Locate every Plasmodium parasite.
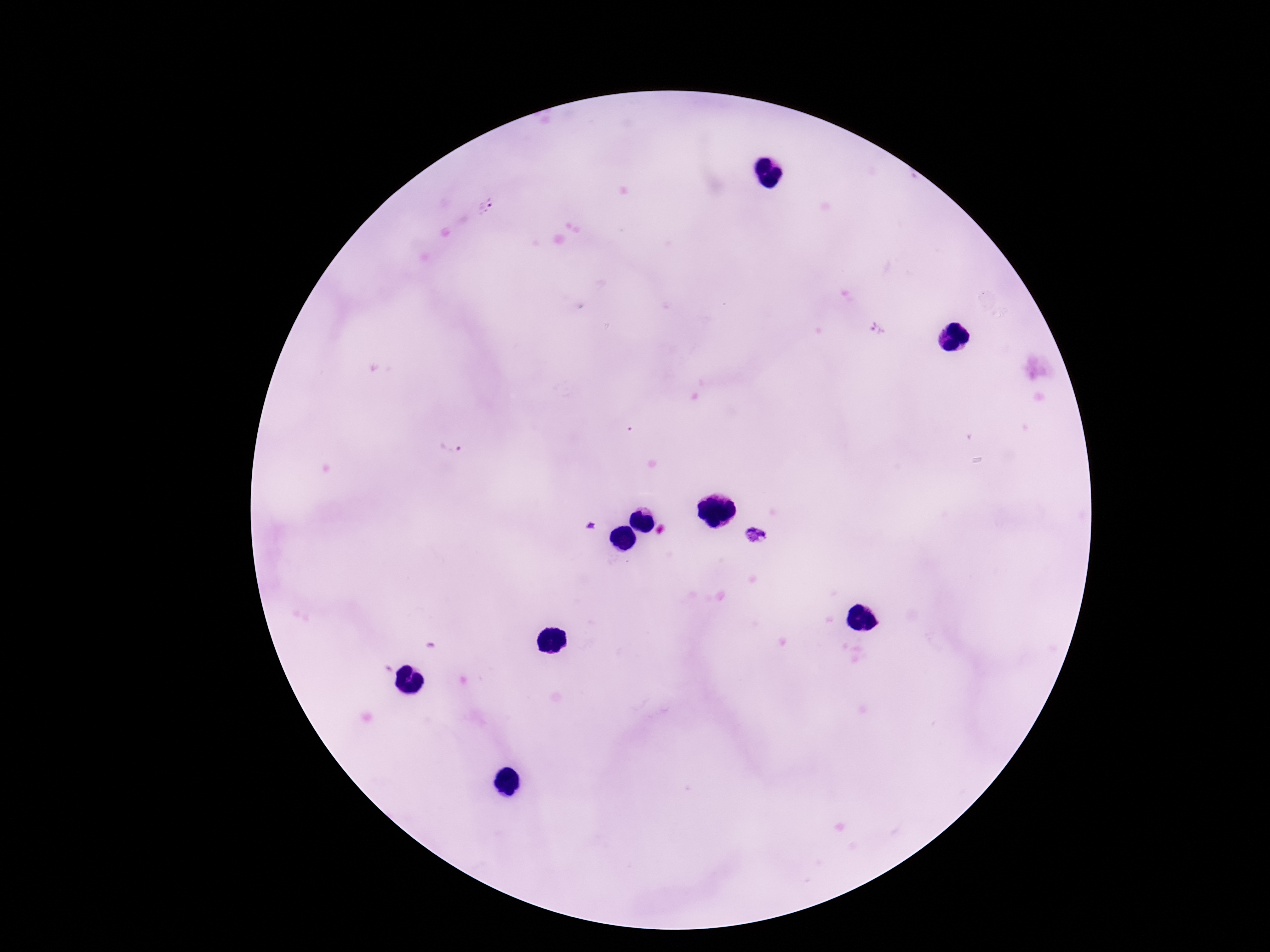
Approximate centers as (x, y) in pixels.
Plasmodium parasites: (486, 206), (878, 331), (447, 449), (591, 524), (754, 535).

field_of_view: one from this slide
stain: Giemsa
patient_malaria_status: infected
capture: smartphone camera through the microscope eyepiece
preparation: thick blood film
magnification: 100x
image_size: 1270×952 pixels